Locate every blood parasite and identify its species.
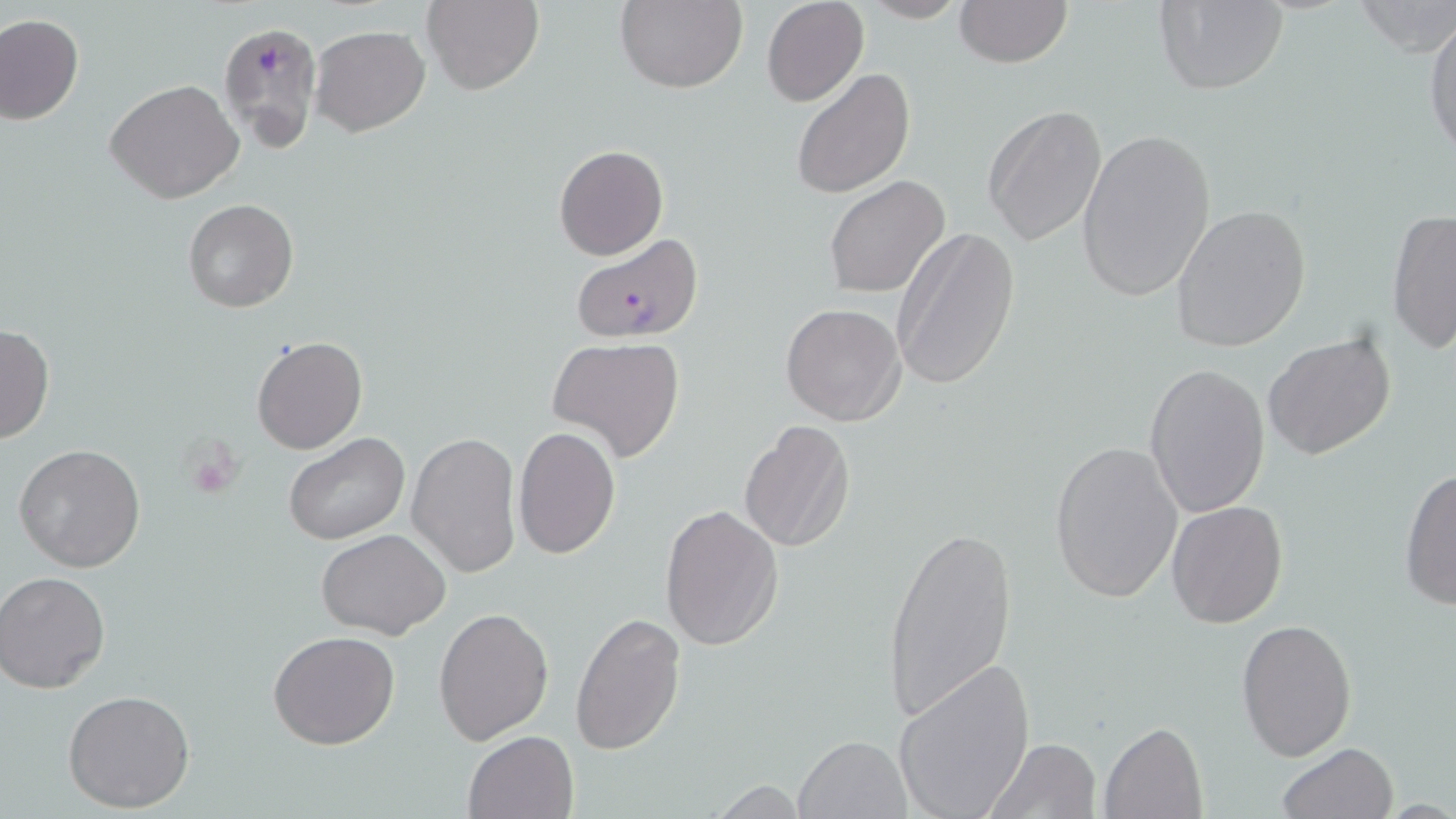

Approximate bounding boxes as named x1/y1/x2/y2 corners in pixels.
Plasmodium falciparum-infected red blood cells: (x1=219, y1=20, x2=322, y2=153), (x1=566, y1=237, x2=701, y2=342).
No Plasmodium ovale, Plasmodium malariae, Plasmodium vivax, Babesia divergens, or Trypanosoma brucei observed.

slide-level diagnosis = Plasmodium falciparum
preparation = thin blood film
uninfected red blood cell locations = approximate bounding boxes as named x1/y1/x2/y2 corners in pixels: (x1=423, y1=0, x2=544, y2=96), (x1=615, y1=0, x2=749, y2=94), (x1=761, y1=0, x2=868, y2=106), (x1=954, y1=0, x2=1072, y2=68), (x1=1153, y1=0, x2=1288, y2=95), (x1=857, y1=1, x2=973, y2=24), (x1=1349, y1=1, x2=1456, y2=54), (x1=0, y1=14, x2=84, y2=125), (x1=1423, y1=16, x2=1456, y2=164), (x1=310, y1=25, x2=430, y2=136), (x1=792, y1=68, x2=916, y2=198), (x1=105, y1=79, x2=243, y2=204), (x1=983, y1=106, x2=1110, y2=249), (x1=1076, y1=127, x2=1217, y2=304), (x1=554, y1=144, x2=669, y2=261), (x1=824, y1=175, x2=950, y2=300), (x1=184, y1=200, x2=298, y2=313), (x1=1170, y1=203, x2=1313, y2=352), (x1=1386, y1=208, x2=1455, y2=354), (x1=890, y1=227, x2=1020, y2=390), (x1=781, y1=303, x2=906, y2=425), (x1=0, y1=323, x2=54, y2=446), (x1=1262, y1=330, x2=1400, y2=463), (x1=252, y1=336, x2=367, y2=455), (x1=546, y1=336, x2=688, y2=465), (x1=1144, y1=362, x2=1271, y2=518), (x1=738, y1=420, x2=855, y2=554), (x1=513, y1=426, x2=623, y2=559), (x1=284, y1=432, x2=412, y2=546), (x1=407, y1=432, x2=521, y2=578), (x1=1048, y1=438, x2=1184, y2=604), (x1=15, y1=444, x2=146, y2=572), (x1=1399, y1=467, x2=1456, y2=612), (x1=1166, y1=501, x2=1288, y2=628), (x1=659, y1=504, x2=784, y2=651), (x1=879, y1=522, x2=1018, y2=726), (x1=317, y1=529, x2=451, y2=640), (x1=1, y1=572, x2=110, y2=693), (x1=433, y1=606, x2=555, y2=745), (x1=570, y1=610, x2=686, y2=755), (x1=1236, y1=618, x2=1358, y2=763), (x1=268, y1=630, x2=401, y2=750), (x1=894, y1=659, x2=1035, y2=818), (x1=64, y1=689, x2=196, y2=813), (x1=1100, y1=721, x2=1208, y2=819), (x1=463, y1=730, x2=580, y2=818), (x1=795, y1=734, x2=910, y2=818), (x1=987, y1=737, x2=1102, y2=818), (x1=1277, y1=742, x2=1399, y2=819), (x1=709, y1=779, x2=810, y2=817)
modality = light microscopy
platelet locations = approximate bounding boxes as named x1/y1/x2/y2 corners in pixels: (x1=179, y1=438, x2=244, y2=500)
magnification = 1000x
field of view = single
image size = 1456×819 pixels
stain = May-Grünwald-Giemsa